Classify this cell by malaria status.
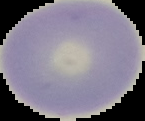

Uninfected.

Summary:
  - Preparation: thin blood smear
  - Image size: 145×121 pixels
  - Image type: segmented cell region on a black background